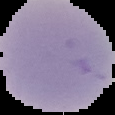

{
  "preparation": "thin blood smear",
  "result": "negative for malaria parasites",
  "image_type": "segmented cell region on a black background",
  "image_size": "115×115 pixels"
}